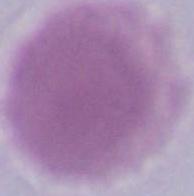

Summary:
  - Modality: photomicrograph
  - Magnification: 1000x
  - Identification: erythrocyte